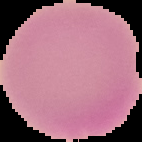

Summary:
  - Image size: 142×142 pixels
  - Image type: segmented cell region on a black background
  - Preparation: thin blood smear
  - Result: no Plasmodium parasites seen